Name the blood parasite species.
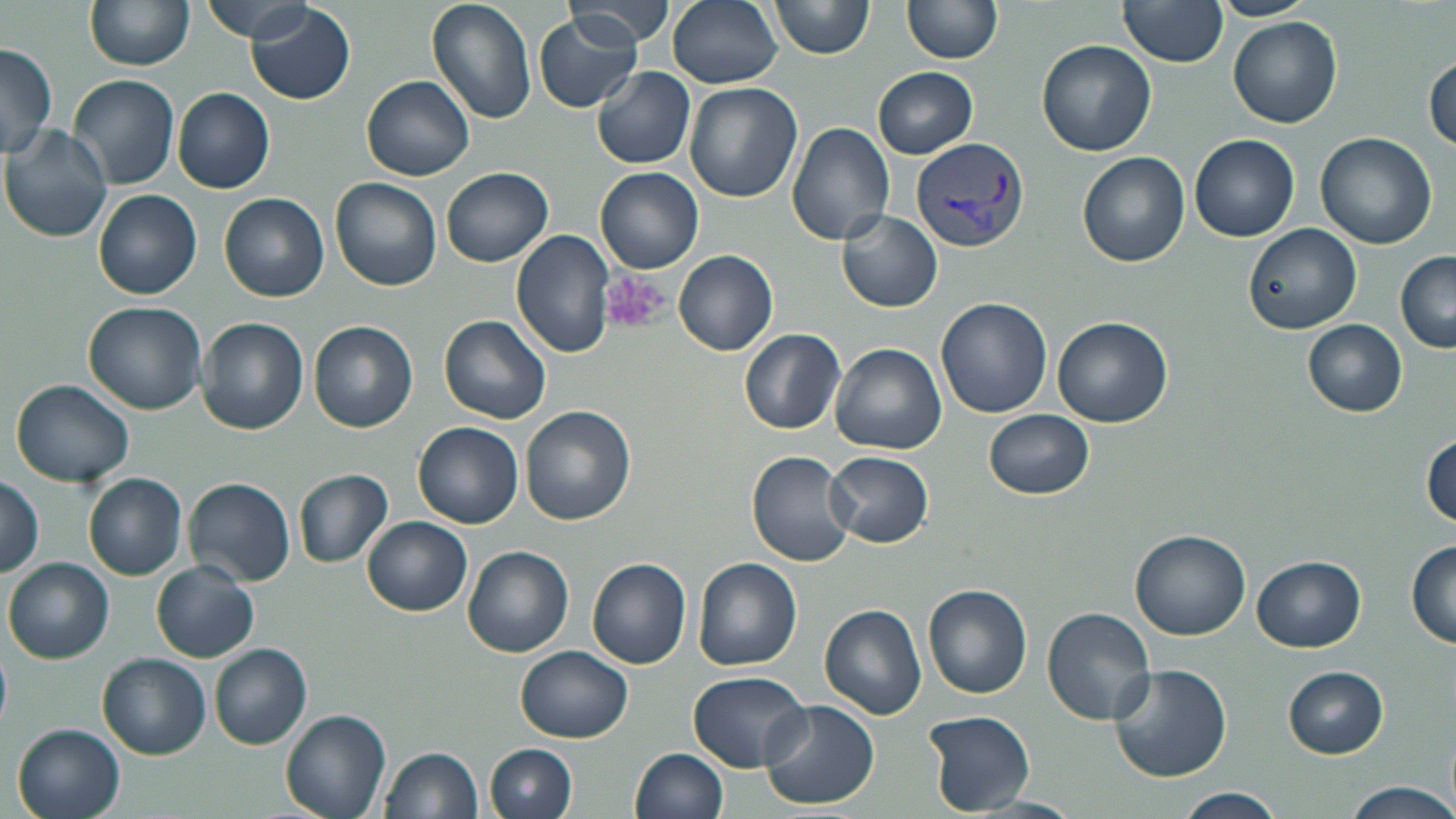

Plasmodium vivax.

{
  "field_of_view": "single",
  "modality": "light microscopy",
  "stain": "May-Grünwald-Giemsa",
  "plasmodium_vivax_infected_red_blood_cell_locations": "approximate bounding boxes as (x1, y1, x2, y2) in pixels: (912, 138, 1029, 254)",
  "preparation": "thin blood smear",
  "uninfected_red_blood_cell_locations": "approximate bounding boxes as (x1, y1, x2, y2) in pixels: (84, 0, 195, 71), (426, 0, 538, 124), (563, 0, 675, 47), (666, 0, 783, 89), (768, 0, 875, 59), (1208, 0, 1318, 21), (204, 1, 320, 44), (901, 1, 1004, 66), (1119, 1, 1228, 69), (246, 3, 356, 106), (533, 13, 642, 112), (1228, 16, 1343, 127), (1037, 39, 1156, 156), (0, 43, 58, 162), (1427, 54, 1456, 156), (591, 66, 696, 170), (873, 66, 978, 158), (68, 74, 179, 189), (362, 74, 476, 181), (686, 82, 801, 203), (172, 88, 275, 194), (786, 122, 896, 245), (1, 124, 115, 241), (1315, 131, 1436, 250), (1189, 132, 1299, 241), (1077, 151, 1191, 267), (595, 167, 704, 274), (442, 168, 552, 267), (331, 177, 442, 291), (93, 189, 203, 298), (220, 192, 329, 302), (838, 211, 943, 313), (1243, 222, 1362, 334), (513, 229, 618, 359), (673, 250, 779, 357), (1396, 252, 1456, 352), (935, 298, 1052, 420), (84, 301, 207, 416), (438, 314, 552, 424), (198, 316, 310, 434), (1053, 318, 1173, 429), (1302, 319, 1408, 416), (309, 321, 418, 433), (739, 328, 846, 435), (830, 342, 946, 456), (10, 378, 135, 488), (520, 405, 637, 525), (985, 409, 1095, 499), (414, 421, 523, 528), (1421, 434, 1455, 529), (825, 450, 933, 547), (747, 451, 856, 567), (294, 470, 394, 568), (84, 473, 188, 580), (0, 475, 44, 577), (187, 478, 295, 586), (362, 516, 472, 616), (1131, 530, 1251, 640), (1406, 541, 1456, 649), (462, 546, 574, 657), (1251, 555, 1365, 653), (6, 557, 114, 664), (588, 558, 692, 669), (694, 558, 802, 671), (152, 562, 259, 661), (923, 583, 1033, 698), (819, 604, 928, 721), (1042, 606, 1157, 725), (0, 638, 11, 732), (209, 644, 313, 749), (517, 645, 633, 743), (98, 655, 210, 758), (1108, 663, 1232, 785), (1284, 666, 1388, 758), (689, 671, 809, 771), (760, 699, 879, 810), (281, 709, 391, 819), (921, 710, 1035, 815), (13, 724, 126, 819), (487, 744, 577, 819), (381, 745, 482, 818), (629, 748, 730, 819), (1340, 780, 1456, 819), (1174, 788, 1287, 819)",
  "image_size": "1456×819 pixels",
  "magnification": "1000x",
  "platelet_locations": "approximate bounding boxes as (x1, y1, x2, y2) in pixels: (601, 272, 667, 334)"
}